Identify the parasite.
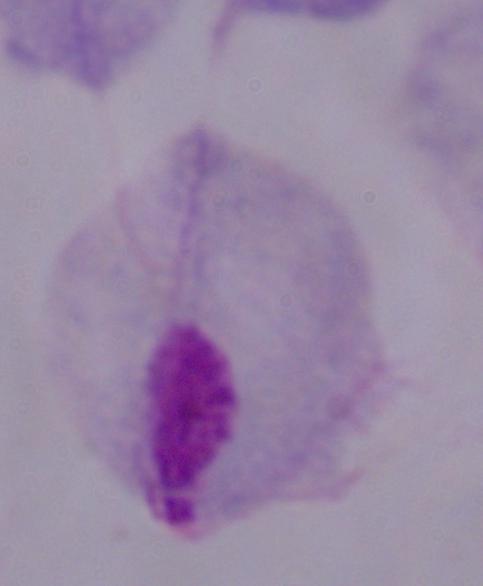

This is a trichomonad.

{
  "magnification": "1000x",
  "modality": "photomicrograph"
}